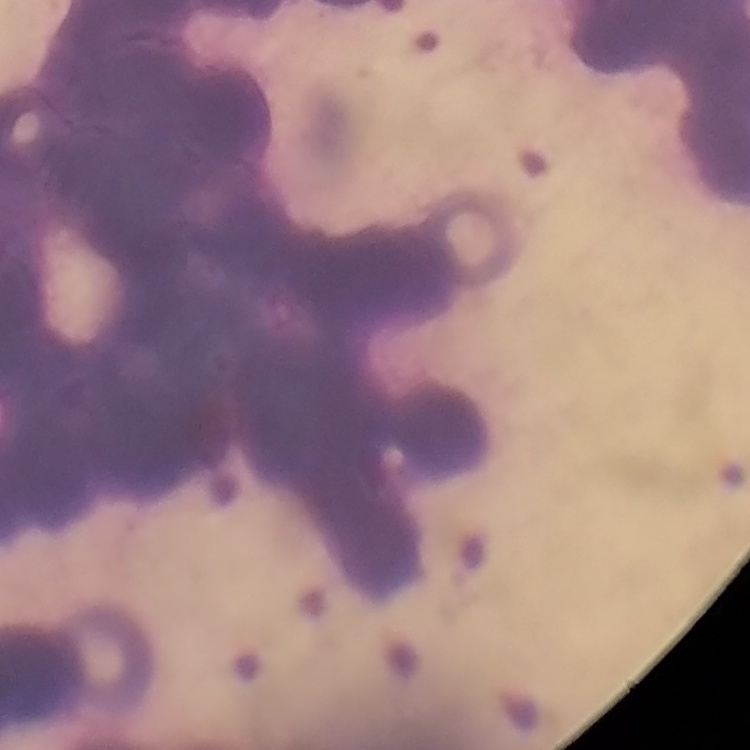

erythrocyte morphology = rouleaux formation
image type = one tile cut from a larger photomicrograph
stain = Field's or Giemsa
preparation = thin peripheral smear